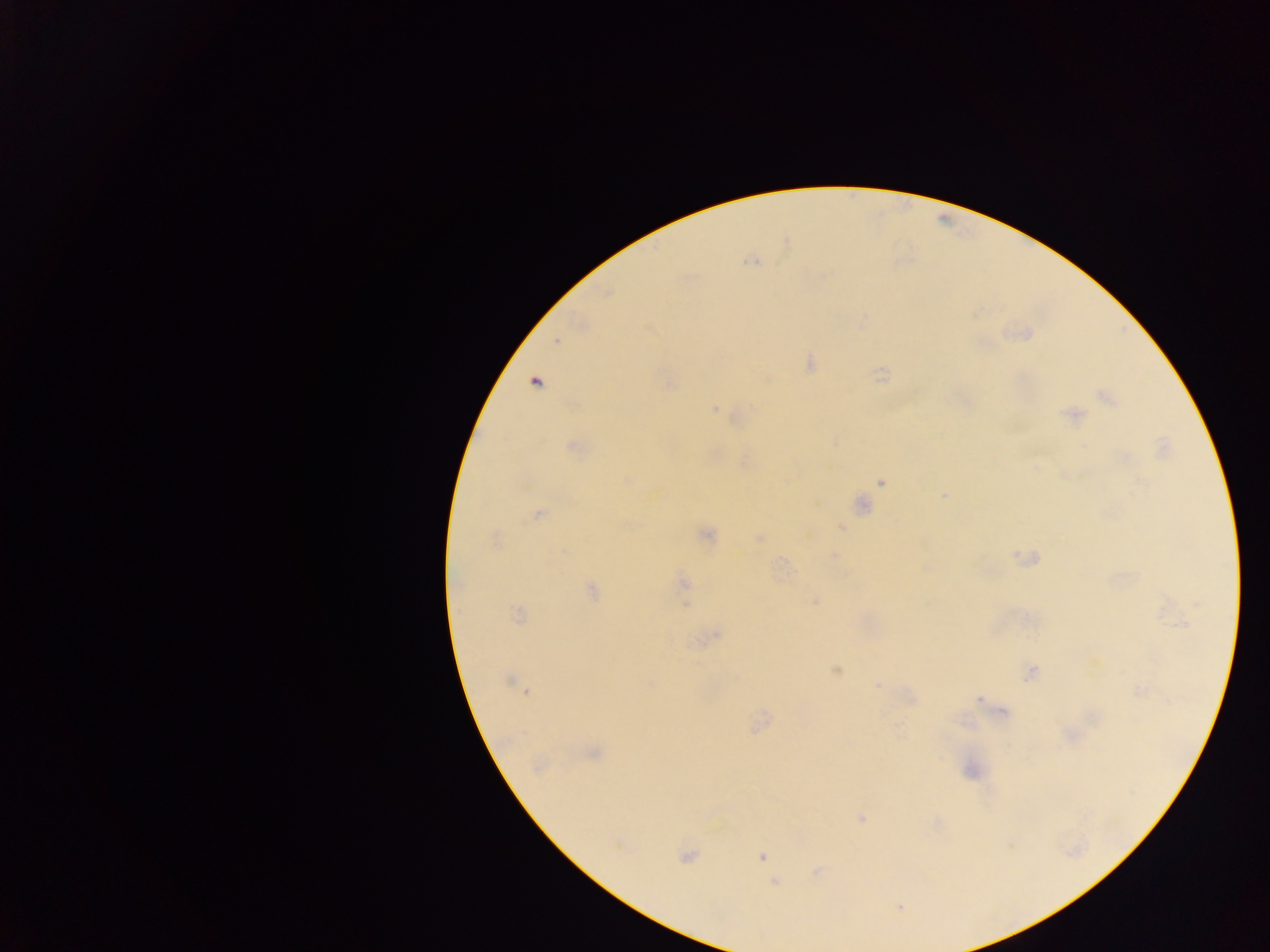 Approximate centers as [x, y] in pixels. Malaria parasite locations: [751, 261], [556, 341], [535, 381], [1105, 396], [715, 409], [1072, 414], [573, 447], [628, 479], [882, 483], [945, 494], [861, 504], [538, 514], [841, 526], [706, 534], [495, 538], [759, 538], [835, 556], [684, 582], [592, 591], [815, 601], [685, 604], [1197, 604], [518, 615], [1181, 624], [716, 635], [835, 670], [1031, 673], [508, 680], [877, 685], [526, 691], [978, 699], [593, 753], [861, 819], [686, 856], [762, 858], [775, 882], [900, 907]. Thick blood film. Image is 1270×952 pixels. Collected in Ghana. Mobile-phone photograph taken through the microscope. Single field of view.